Report the malaria status of this cell.
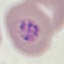

It is parasitized.

Thin blood smear. Acquired by smartphone through the microscope eyepiece. Giemsa stain. Cell patch, automatically extracted from a larger field of view and resized to 64 × 64 pixels.